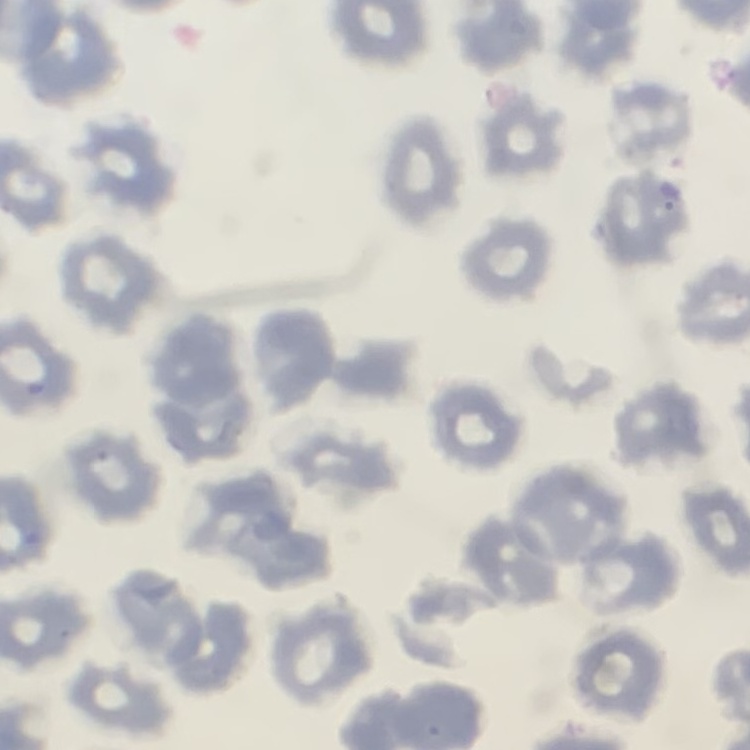
Summary:
  - Red blood cell morphology: no rouleaux formation
  - Stain: Field's or Giemsa
  - Image type: square crop of a larger photomicrograph
  - Preparation: thin peripheral smear